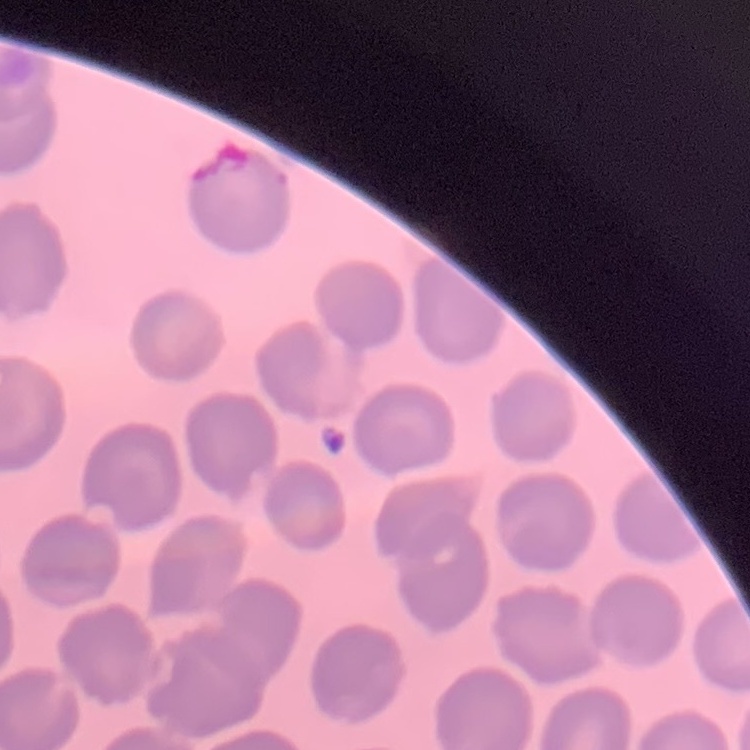

Summary:
  - Red blood cell morphology: no rouleaux formation
  - Stain: Field's or Giemsa
  - Preparation: thin blood film
  - Image type: square crop of a larger photomicrograph